Assess this cell for malaria.
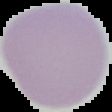
Uninfected.

From a thin blood film. Cell region segmented out of the field of view; the surrounding area is masked to black. Image is 112×112 pixels.